Classify this cell by malaria status.
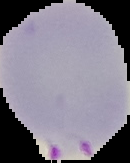

It is parasitized.

Cell region segmented out of the field of view; the surrounding area is masked to black. From a thin blood film. Image is 130×163 pixels.